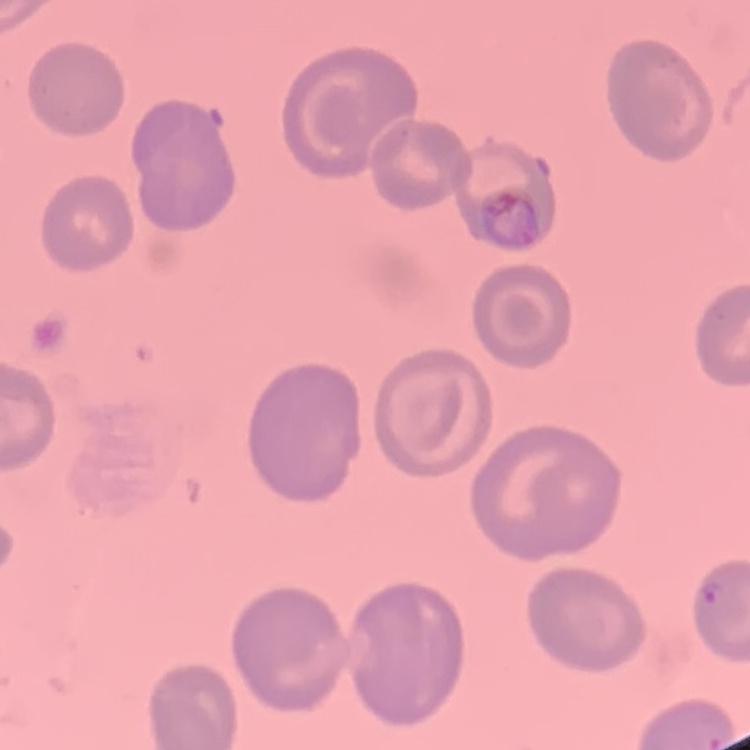

Summary:
  - Erythrocyte morphology: no rouleaux formation
  - Image type: one tile cut from a larger photomicrograph
  - Preparation: thin blood smear
  - Stain: Field's or Giemsa